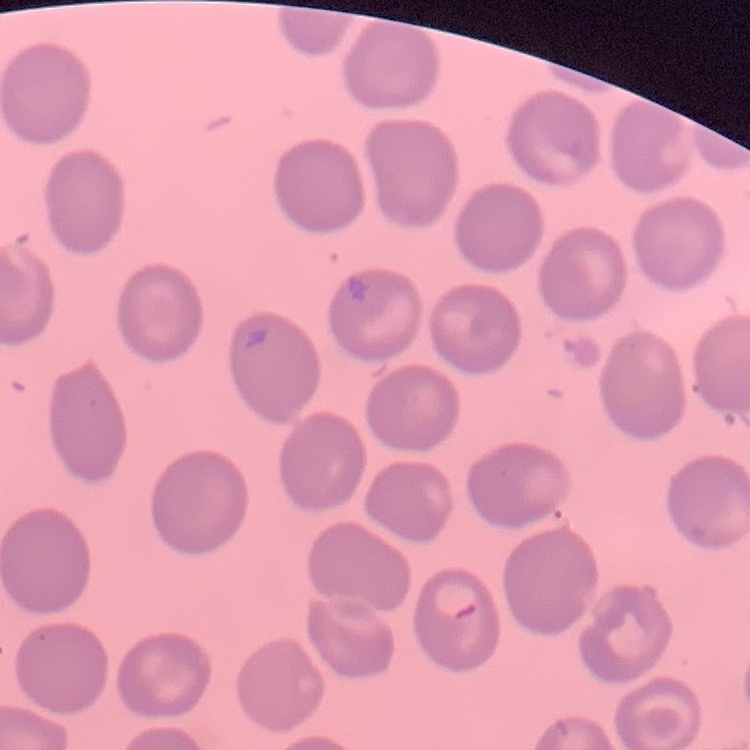

Summary:
  - Red blood cell morphology: no rouleaux formation
  - Preparation: thin blood film
  - Image type: square crop of a larger photomicrograph
  - Stain: Field's or Giemsa